Classify this cell by malaria status.
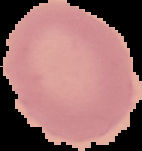
It is uninfected.

image type = segmented cell region on a black background
image size = 142×151 pixels
preparation = thin blood smear